Identify the blood parasite species.
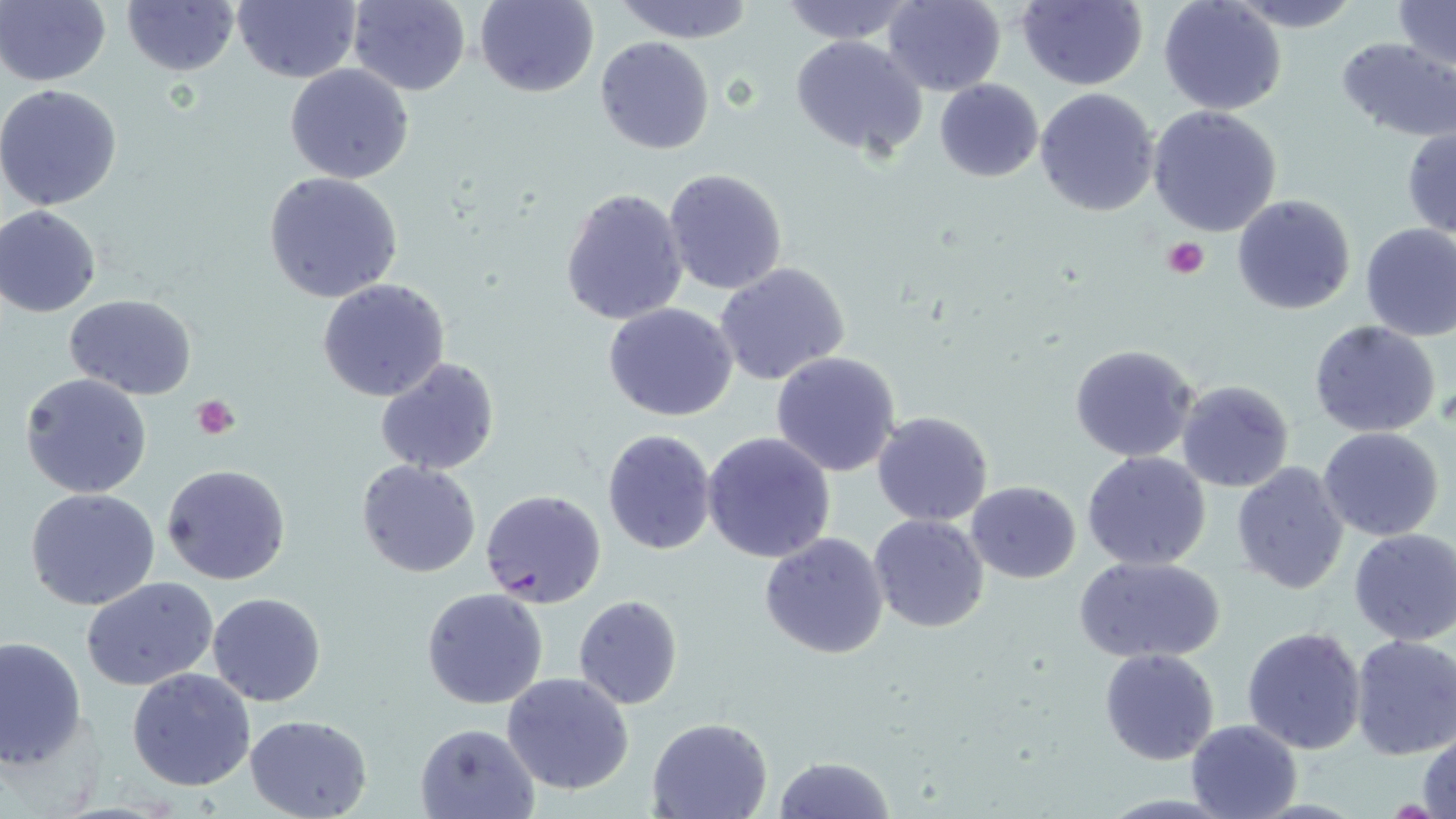
Plasmodium falciparum.

Summary:
  - Coordinate format: approximate bounding boxes as (x1,y1)-(x2,y2) corner pairs in pixels
  - Platelet locations: (1163,236)-(1209,279), (190,396)-(239,440)
  - Plasmodium falciparum-infected red blood cell locations: (479,488)-(606,610)
  - Uninfected red blood cell locations: (121,0)-(240,75), (234,0)-(361,84), (346,0)-(472,95), (475,0)-(599,98), (881,0)-(1007,97), (1015,0)-(1148,91), (1224,0)-(1366,32), (0,1)-(110,87), (613,1)-(757,43), (776,1)-(916,45), (1158,1)-(1287,115), (1392,1)-(1455,72), (790,35)-(928,159), (594,37)-(715,156), (1335,37)-(1455,141), (285,63)-(415,184), (934,78)-(1044,183), (0,83)-(124,212), (1034,87)-(1161,216), (1147,105)-(1283,236), (1402,125)-(1456,238), (662,168)-(789,296), (263,171)-(405,303), (559,187)-(689,326), (1232,193)-(1357,315), (0,207)-(103,317), (1358,222)-(1456,341), (715,263)-(852,387), (317,278)-(450,402), (64,294)-(197,401), (604,304)-(739,422), (1308,320)-(1441,439), (1068,343)-(1201,464), (770,352)-(903,478), (374,357)-(500,476), (20,372)-(152,498), (1176,379)-(1294,494), (870,410)-(995,527), (603,428)-(716,554), (1317,428)-(1445,541), (702,432)-(837,563), (1082,451)-(1212,570), (355,459)-(481,578), (1231,461)-(1351,595), (161,463)-(292,586), (966,480)-(1081,584), (27,487)-(161,610), (868,513)-(990,634), (1348,529)-(1456,646), (757,531)-(888,661), (1075,555)-(1224,664), (81,576)-(221,690), (422,588)-(549,710), (207,592)-(327,706), (573,594)-(683,709), (1242,626)-(1368,755), (0,634)-(86,769), (1348,634)-(1456,760), (1099,648)-(1220,765), (127,667)-(256,790), (501,671)-(634,794), (245,714)-(373,819), (648,717)-(773,818), (1185,719)-(1304,819), (414,723)-(540,818), (1417,728)-(1455,818), (773,754)-(894,819)
  - Field of view: single
  - Modality: optical microscopy
  - Image size: 1456×819 pixels
  - Magnification: 1000x
  - Preparation: thin blood smear
  - Stain: May-Grünwald-Giemsa